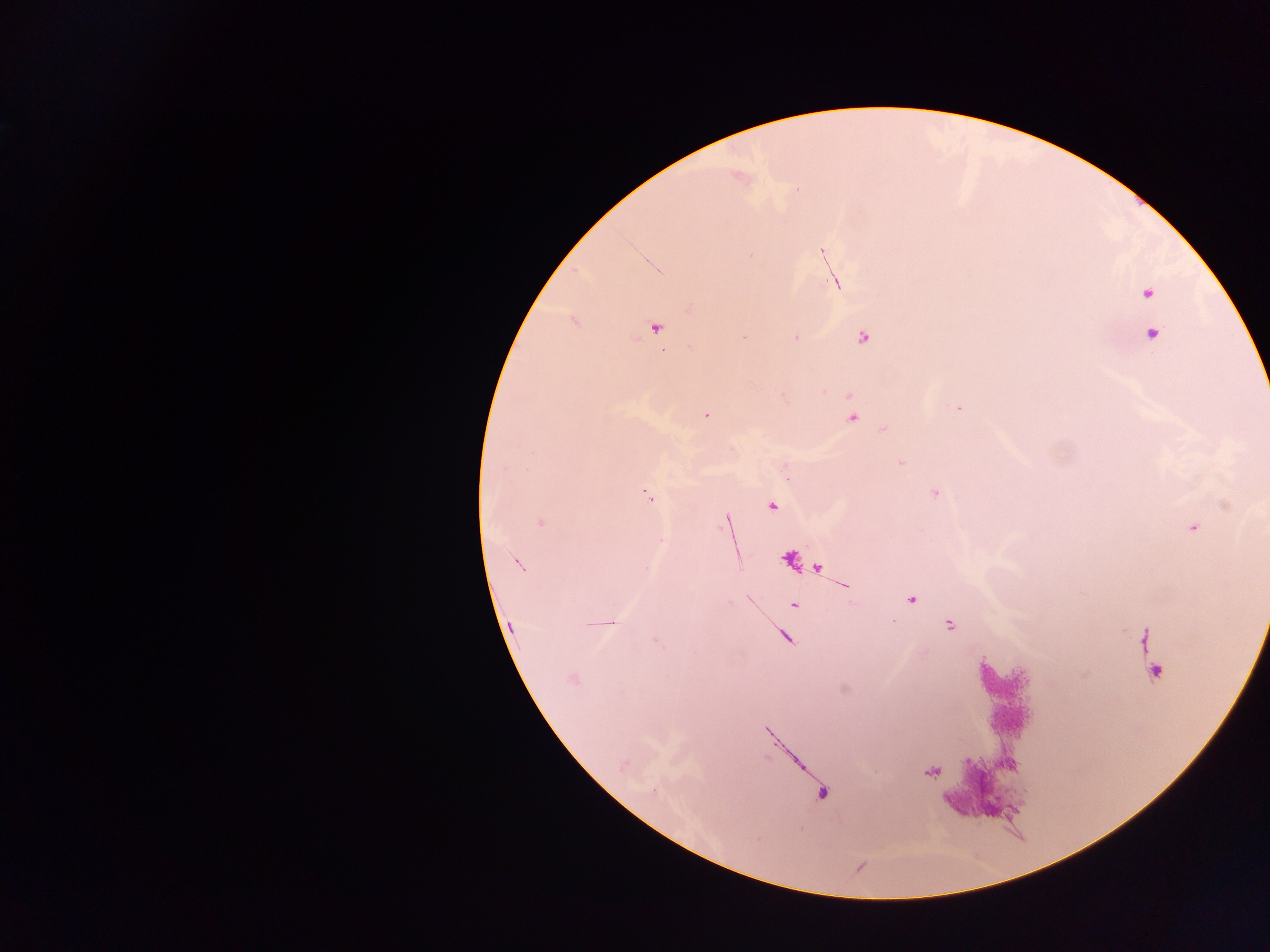
Approximate centers as x y in pixels. Plasmodium parasite locations: 738 176; 822 252; 750 255; 836 282; 1147 293; 689 309; 656 327; 1152 334; 795 337; 744 338; 863 338; 959 408; 706 416; 852 418; 884 429; 900 462; 505 467; 935 493; 648 496; 772 506; 726 520; 540 523; 1194 527; 661 540; 518 564; 911 599; 793 605; 604 623; 949 625; 1146 638; 656 642; 1149 652; 1155 672; 573 679; 623 765; 932 772. Photographed through a microscope with a mobile-phone camera. Single field of view. Image is 1270×952 pixels. Thick blood film. Collected in Ghana.